Classify this cell by malaria status.
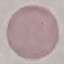
It is uninfected.

{
  "image_type": "automatically extracted cell patch, resized to 64 × 64 pixels",
  "preparation": "thin blood film",
  "stain": "Giemsa",
  "capture": "smartphone through the microscope eyepiece"
}